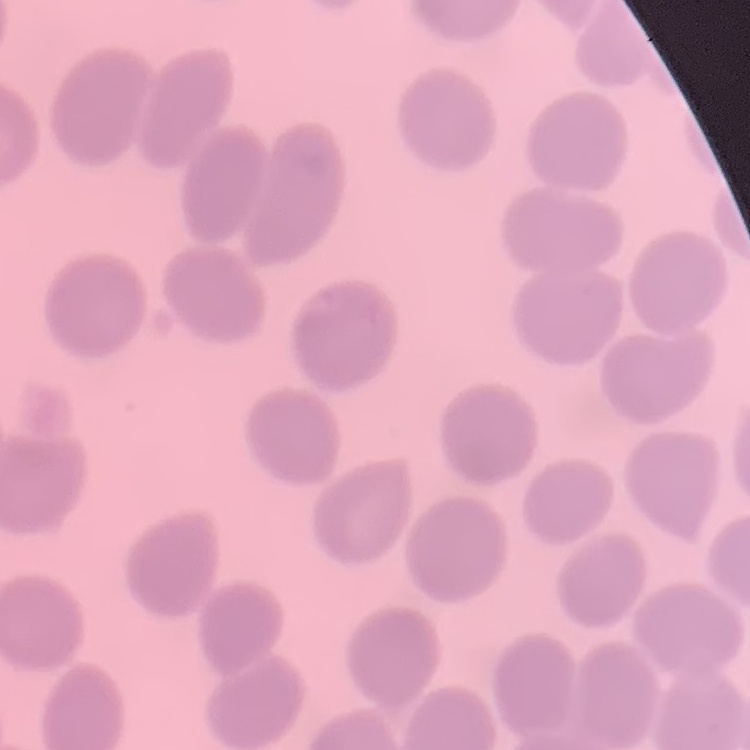

The red blood cells exhibit no rouleaux formation. Thin blood smear. Square crop of a larger photomicrograph. Stained with either Field's or Giemsa.